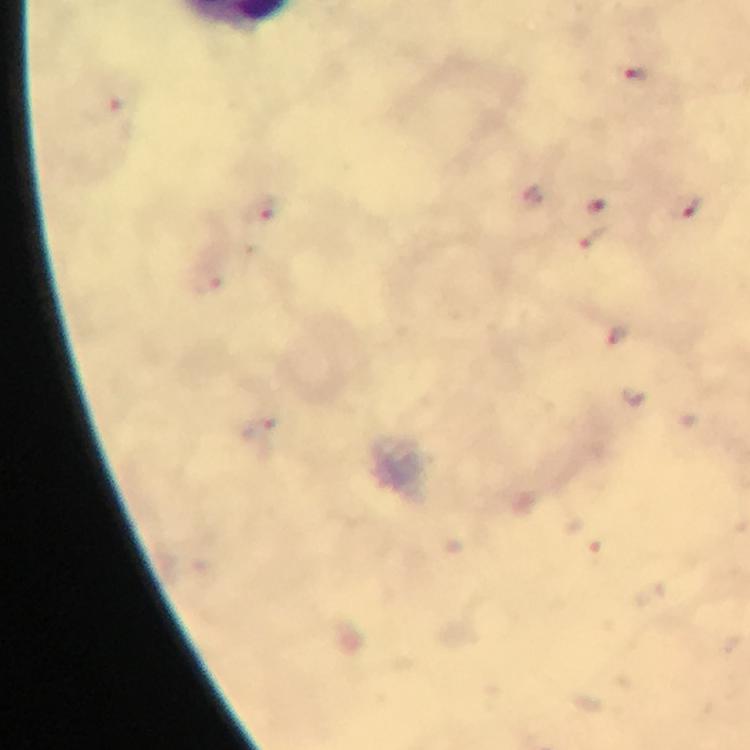
context = from a diagnostic examination for malaria
stain = Giemsa
preparation = thick blood smear
image size = 750×750 pixels
capture = smartphone photograph through a microscope
magnification = 100x
cropped from = one field of view
immersion oil = used
malaria parasite locations = approximate centers as (x, y) in pixels: (638, 74), (104, 109), (594, 206), (688, 208), (268, 212), (598, 239)